Name the parasite shown.
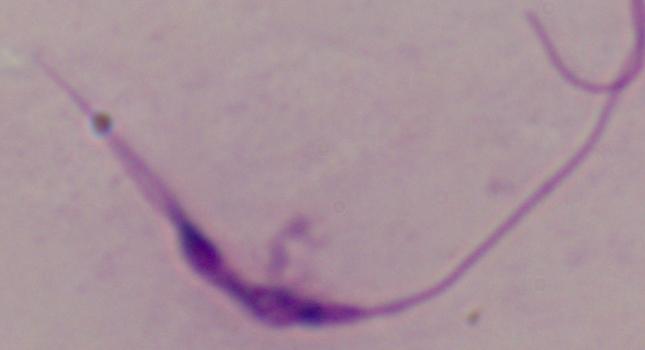

Leishmania.

modality = photomicrograph
magnification = 1000x